Report the malaria status of this cell.
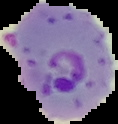

Parasitized.

Image is 118×124 pixels. From a thin blood film. The area outside the segmented cell region is set to black.